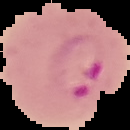

Summary:
  - Image size: 130×130 pixels
  - Image type: segmented cell region with the area outside set to black
  - Result: malaria parasites identified
  - Preparation: thin blood film